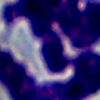

Summary:
  - Modality: photomicrograph
  - Magnification: 1000x
  - Identification: white blood cell